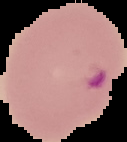

Malaria status: parasitized. From a thin blood film. Image is 127×142 pixels. Segmented cell region on a black background.